State which parasite is depicted.
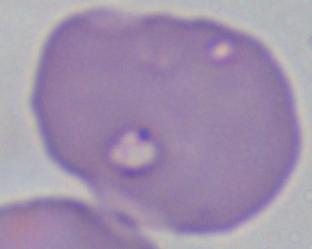

Babesia.

Summary:
  - Magnification: 1000x
  - Modality: micrograph